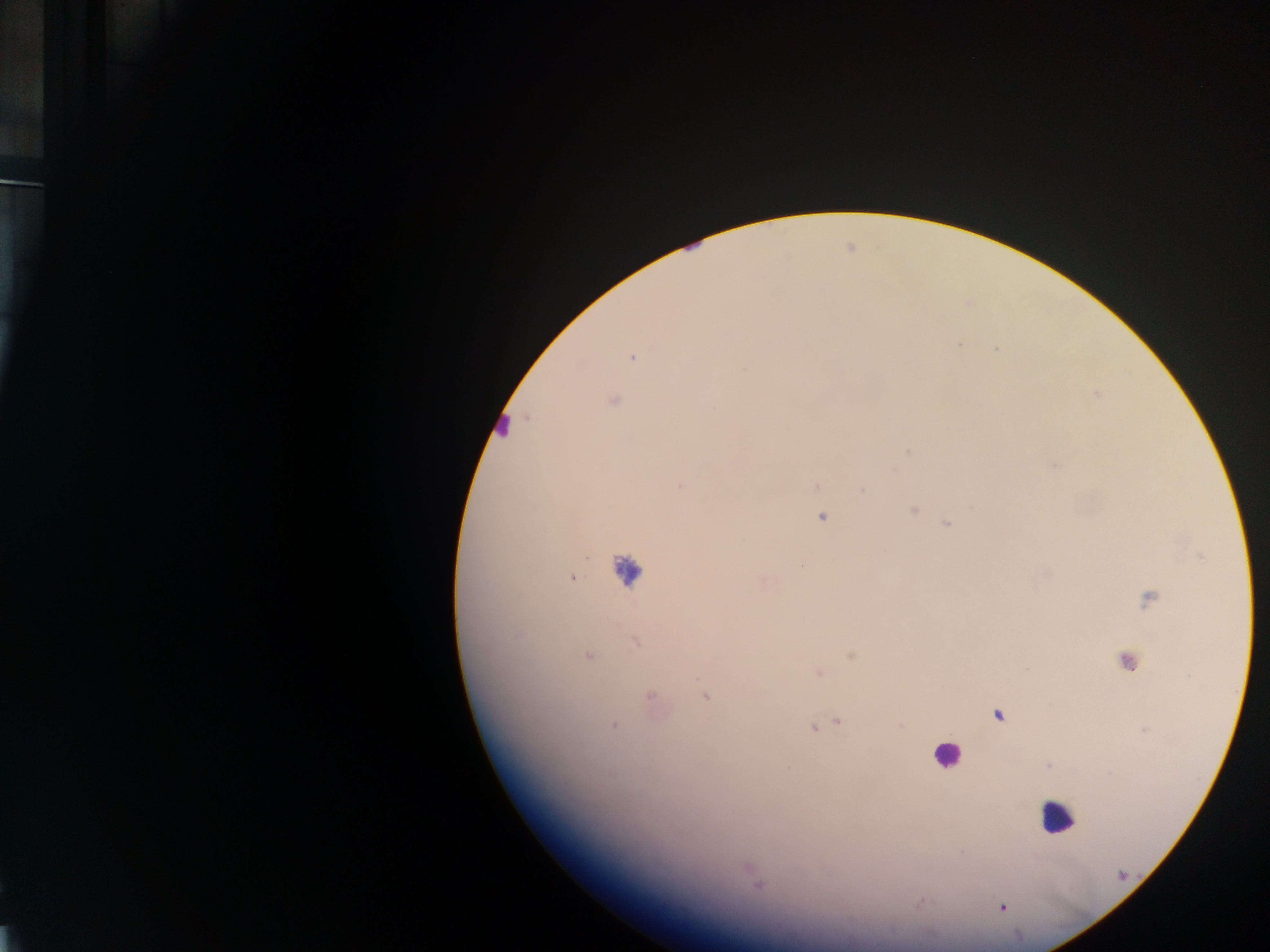
Approximate centers as [x, y] in pixels. Plasmodium parasite locations: [996, 349], [632, 357], [614, 400], [907, 451], [1054, 466], [680, 486], [817, 486], [863, 490], [913, 510], [822, 517], [947, 524], [801, 565], [571, 578], [1150, 598], [635, 642], [588, 656], [1128, 661], [650, 697], [705, 697], [837, 722], [613, 724], [813, 728], [757, 887], [1002, 907]. Leukocyte locations (subset; some below the resolvable size): [500, 421], [626, 569], [946, 756], [1057, 816]. Thick blood film. One field of view. Image is 1270×952 pixels. Photographed through a microscope with a mobile-phone camera. Collected in Ghana.